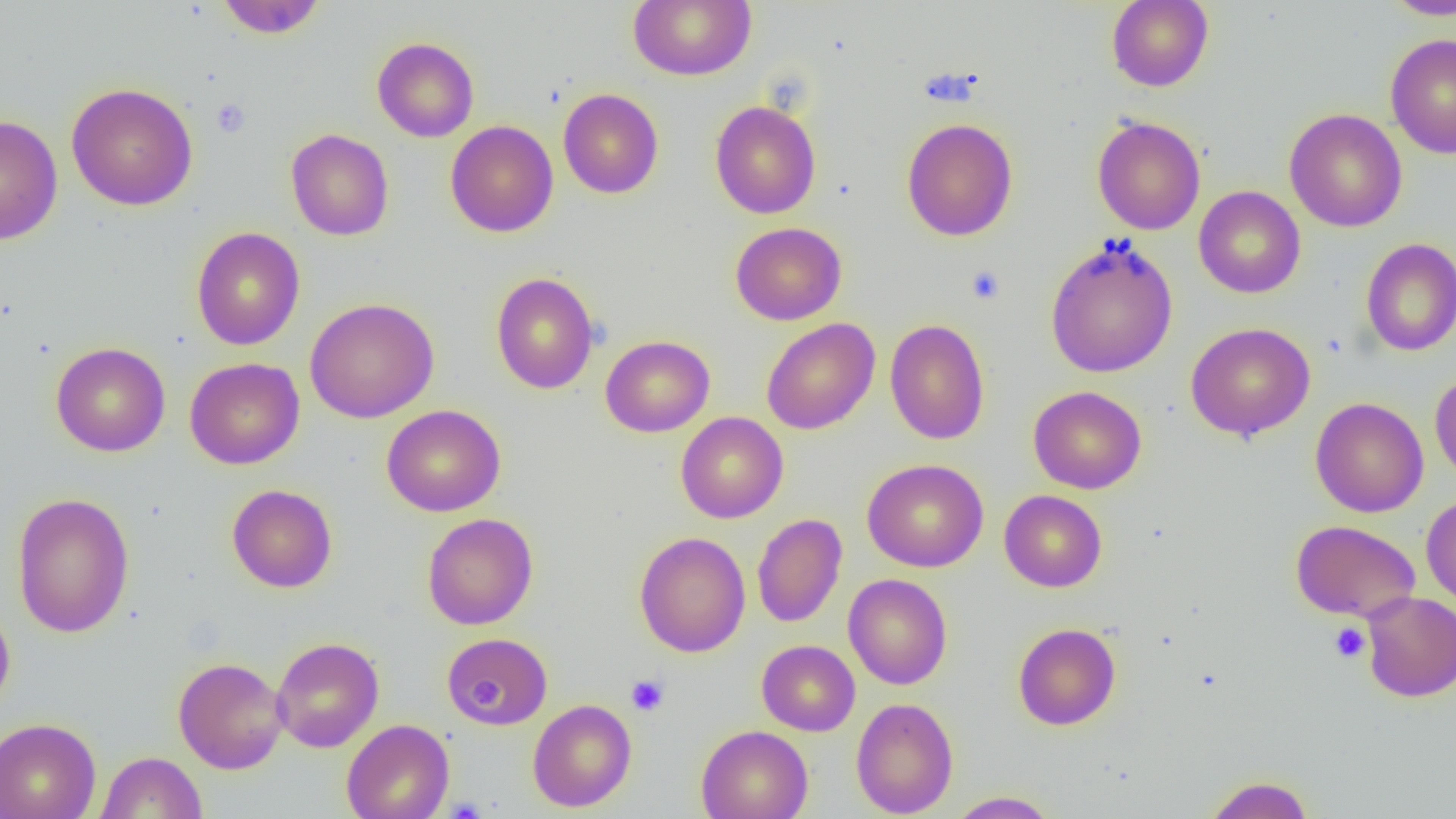
Summary:
  - Coordinate format: approximate bounding boxes as [x1, y1, x2, y2] in pixels
  - Platelet locations: [211, 98, 251, 138], [966, 266, 1005, 304], [1329, 622, 1370, 663], [626, 674, 670, 716], [443, 798, 488, 819]
  - Uninfected red blood cell locations: [215, 0, 327, 38], [628, 0, 756, 81], [1106, 0, 1214, 92], [1380, 0, 1456, 20], [1386, 34, 1456, 158], [372, 37, 479, 142], [66, 82, 198, 211], [558, 88, 664, 199], [710, 100, 821, 219], [1284, 108, 1407, 232], [0, 115, 63, 245], [1092, 116, 1206, 235], [901, 117, 1018, 241], [445, 120, 559, 238], [286, 128, 394, 241], [1194, 186, 1305, 298], [731, 222, 847, 325], [191, 227, 305, 350], [1045, 236, 1178, 378], [1360, 238, 1456, 356], [491, 272, 599, 394], [305, 298, 439, 423], [761, 318, 880, 435], [885, 319, 990, 445], [1186, 322, 1315, 441], [600, 335, 715, 437], [50, 341, 171, 457], [185, 357, 304, 470], [1430, 370, 1456, 487], [1028, 386, 1146, 494], [1310, 397, 1428, 517], [381, 404, 506, 517], [675, 412, 788, 523], [862, 459, 989, 572], [227, 484, 337, 593], [999, 490, 1107, 592], [12, 492, 135, 638], [1421, 494, 1456, 610], [422, 513, 538, 630], [752, 513, 847, 628], [1291, 520, 1420, 621], [634, 531, 751, 657], [843, 574, 952, 690], [1361, 592, 1455, 702], [0, 602, 15, 715], [1013, 622, 1121, 730], [441, 632, 553, 730], [270, 637, 384, 752], [757, 640, 860, 736], [173, 657, 288, 774], [851, 697, 958, 818], [527, 699, 637, 811], [0, 718, 101, 819], [341, 719, 454, 819], [695, 725, 813, 819], [96, 751, 207, 818], [1203, 774, 1316, 818], [948, 790, 1060, 818]
  - Slide-level diagnosis: negative for blood parasites
  - Magnification: 1000x
  - Modality: optical microscopy
  - Preparation: thin blood smear
  - Image size: 1456×819 pixels
  - Field of view: one of a larger specimen